Assess this cell for malaria.
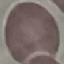

Uninfected.

capture = smartphone camera at the microscope eyepiece
image type = cell patch, automatically extracted from a larger field of view and resized to 64 × 64 pixels
stain = Giemsa
preparation = thin blood smear